State which cell type is depicted.
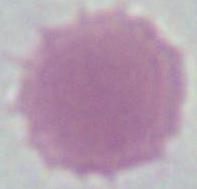
An erythrocyte.

Micrograph. Captured at 1000x magnification.